Point out each malaria parasite.
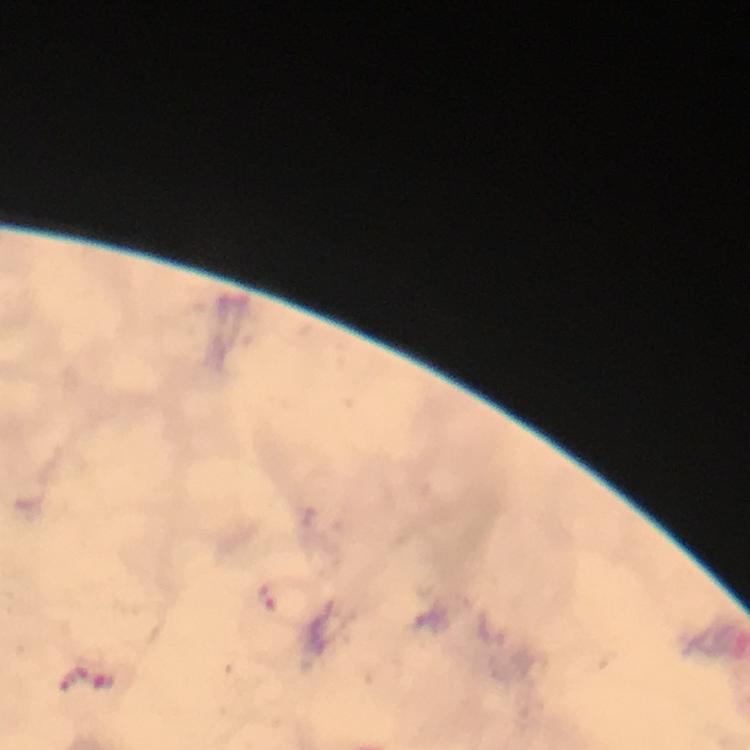
Approximate centers as [x, y] in pixels.
Malaria parasites: [266, 593].

capture = smartphone mounted on the microscope
preparation = thick blood smear
stain = Giemsa
cropped from = a single field of view
context = from a malaria diagnostic workup
image size = 750×750 pixels
magnification = 100x
immersion oil = applied